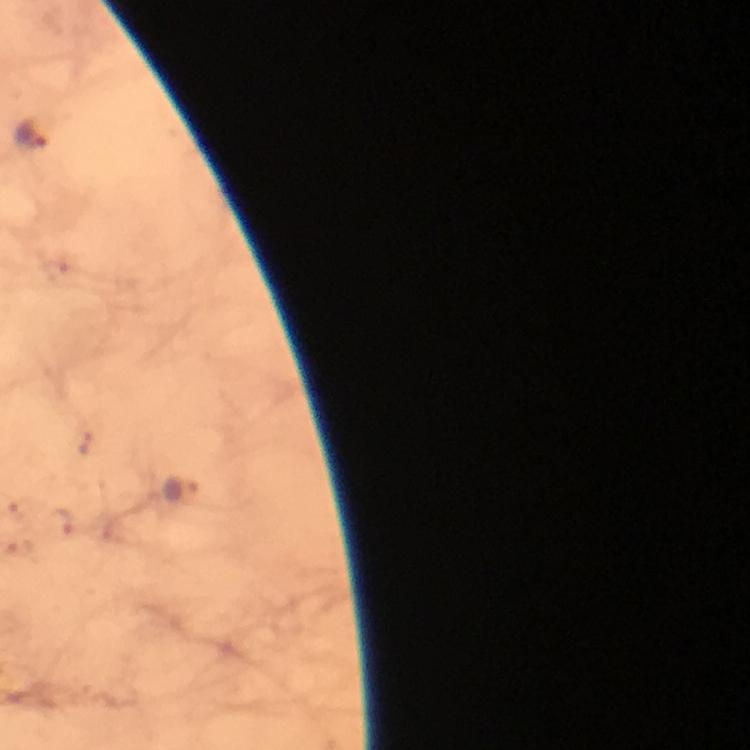

cropped from = a single field of view
stain = Giemsa
magnification = 100x
capture = smartphone mounted on the microscope
immersion oil = used
context = from a malaria diagnostic workup
preparation = thick blood smear
image size = 750×750 pixels
Plasmodium parasite locations = approximate centers as {x, y} in pixels: {31, 135}, {56, 273}, {87, 443}, {180, 492}, {23, 509}, {61, 522}